Report the malaria status of this cell.
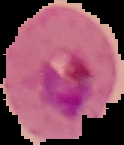

Parasitized.

image type = segmented cell region with the area outside set to black
preparation = thin blood smear
image size = 124×145 pixels